Name the parasite shown.
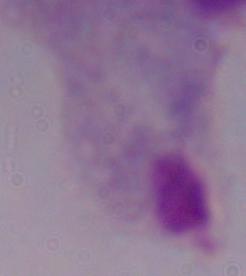

A trichomonad.

Captured at 1000x magnification. Micrograph.